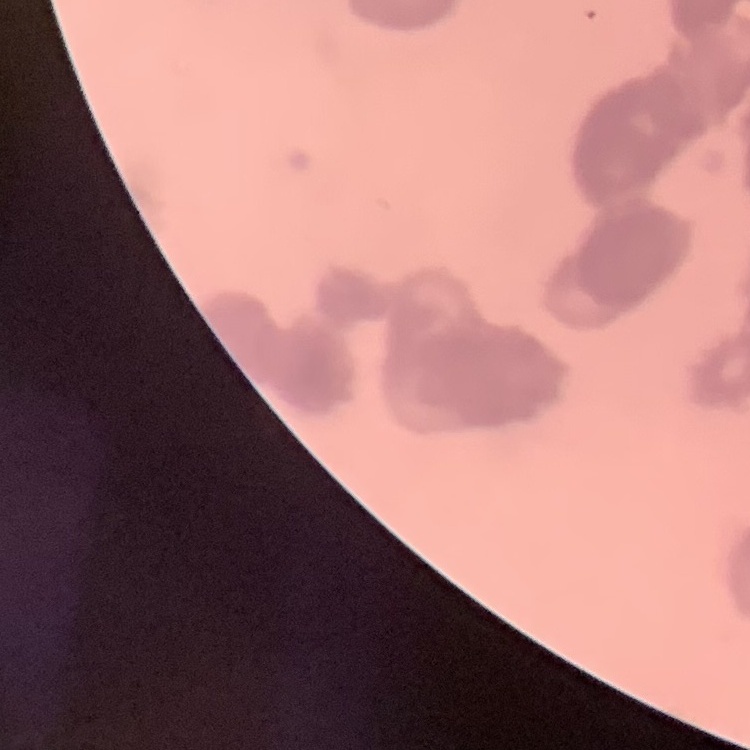
The red blood cells exhibit rouleaux formation. Field's or Giemsa stain. One tile cut from a larger photomicrograph. Thin blood smear.